Identify the preparation type.
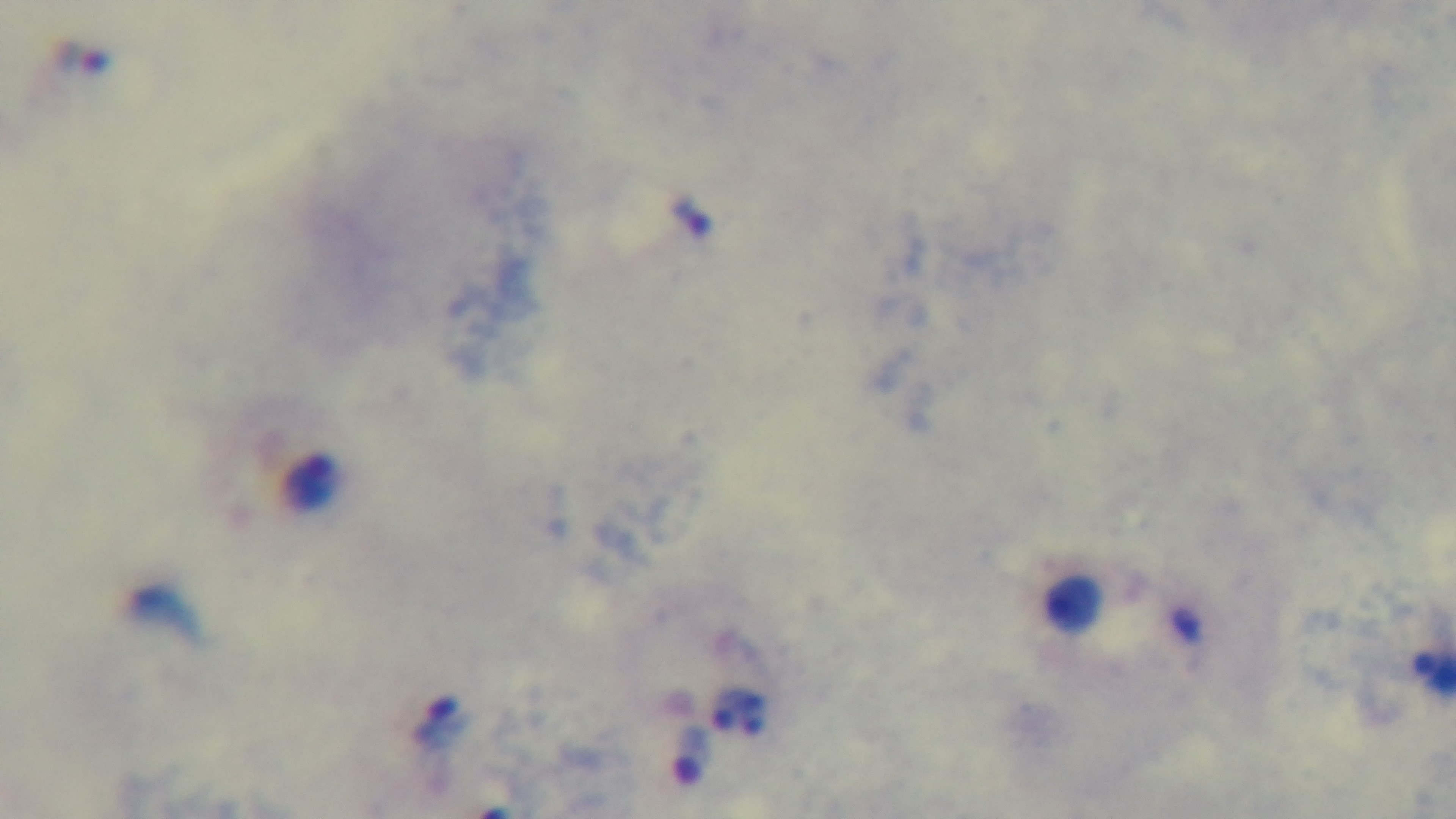
It is a thick blood film.

malaria status = infected
capture = mounted 4K digital camera
modality = light microscopy
stain = Giemsa
field of view = one from the slide
objective = 100x oil immersion